Locate every blood parasite and identify its species.
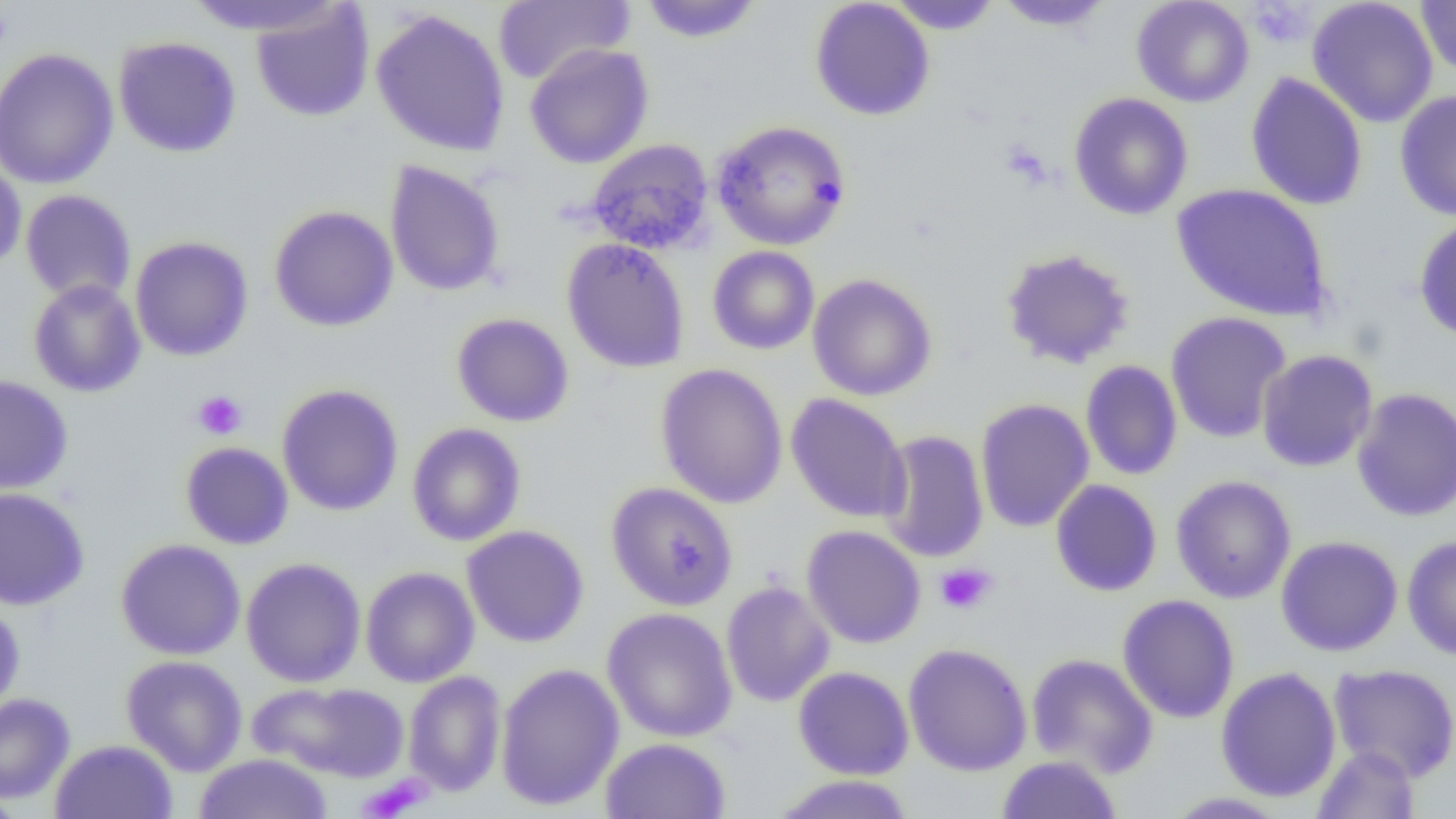

No blood parasites observed.

Approximate bounding boxes as (x1,y1)-(x2,y2) corner pairs in pixels. Platelet locations: (1247,2)-(1314,49), (192,390)-(247,440), (934,562)-(997,615), (358,775)-(432,818). Uninfected red blood cell locations: (491,0)-(635,85), (638,0)-(764,43), (810,0)-(935,121), (885,0)-(1004,35), (1131,0)-(1254,107), (1307,0)-(1438,128), (182,1)-(349,37), (992,1)-(1115,31), (1415,1)-(1456,78), (250,3)-(375,122), (370,8)-(511,157), (113,36)-(242,158), (524,43)-(654,169), (0,47)-(119,190), (1245,72)-(1368,211), (1394,90)-(1456,221), (1068,92)-(1194,220), (711,119)-(851,251), (586,138)-(715,254), (0,156)-(27,274), (384,160)-(506,297), (1171,183)-(1333,322), (20,189)-(137,305), (269,205)-(399,332), (1413,216)-(1456,343), (129,235)-(254,362), (561,238)-(690,373), (707,245)-(819,355), (1000,247)-(1136,369), (808,273)-(937,401), (28,279)-(146,397), (1165,311)-(1292,444), (451,312)-(574,427), (1257,349)-(1378,472), (1080,360)-(1183,481), (655,363)-(789,509), (0,374)-(73,495), (276,384)-(404,516), (1352,387)-(1456,523), (785,393)-(911,524), (975,398)-(1094,533), (406,423)-(526,546), (877,429)-(989,563), (180,441)-(294,550), (1171,475)-(1297,604), (1050,479)-(1162,596), (606,481)-(739,611), (0,487)-(90,610), (461,525)-(589,648), (802,525)-(926,648), (1276,535)-(1403,656), (1402,535)-(1456,660), (115,538)-(246,661), (241,557)-(367,687), (361,566)-(480,688), (721,580)-(835,708), (1117,594)-(1240,724), (0,598)-(26,717), (601,607)-(738,742), (902,643)-(1033,777), (1026,653)-(1159,778), (121,655)-(248,776), (495,663)-(625,810), (1328,664)-(1456,782), (793,666)-(915,781), (1215,667)-(1342,802), (403,670)-(507,796), (249,680)-(410,782), (0,693)-(75,804), (600,738)-(732,819), (50,739)-(178,818), (1311,744)-(1420,818), (193,753)-(334,818), (996,755)-(1123,818), (769,774)-(917,818), (0,787)-(25,819), (1163,792)-(1291,818). Slide-level diagnosis: negative for blood parasites. Image is 1456×819 pixels. Single field of view. Light microscopy. 1000x magnification. Thin blood smear.